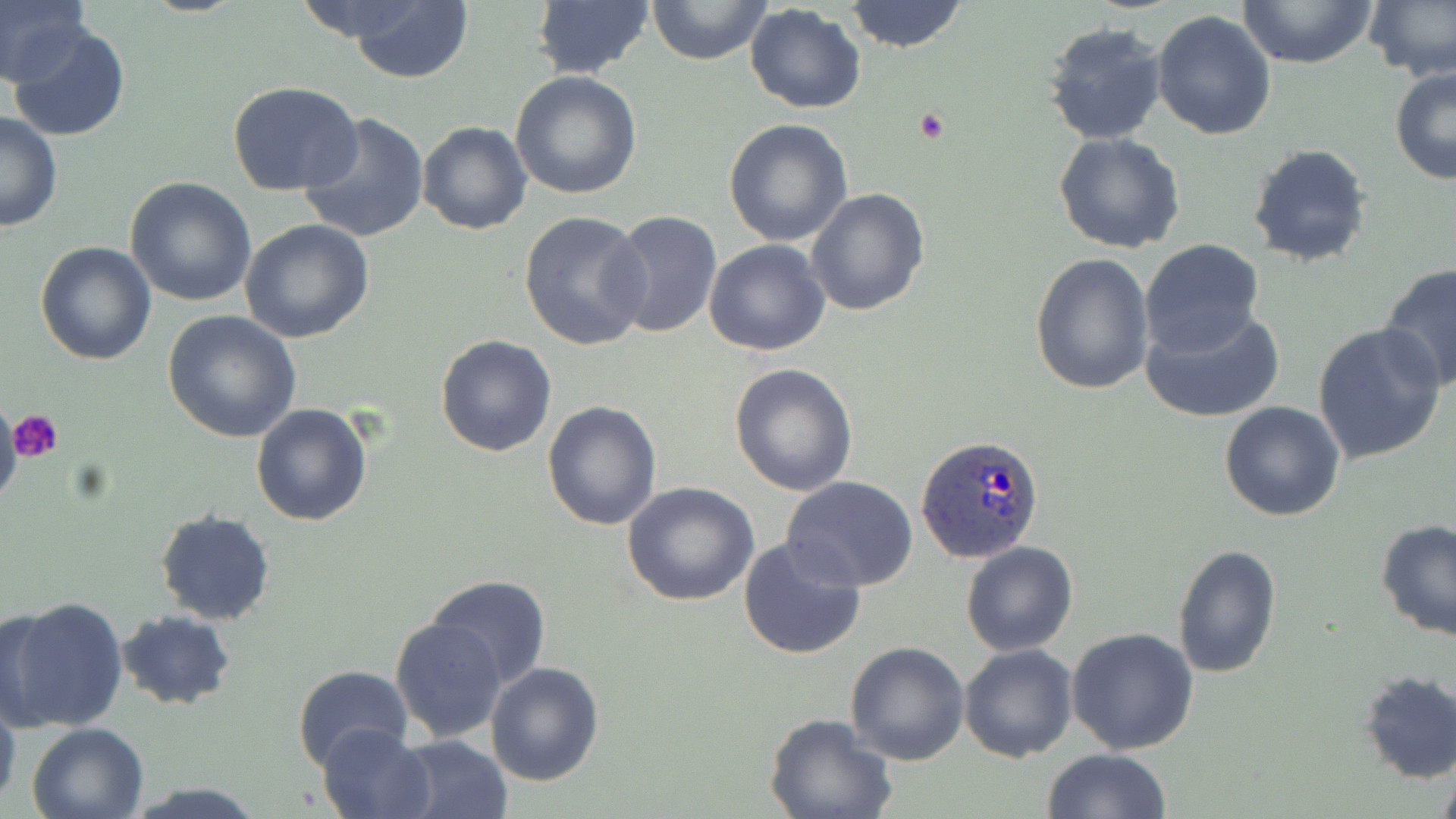
Summary:
  - Coordinate format: approximate bounding boxes as named x1/y1/x2/y2 corners in pixels
  - Plasmodium ovale-infected red blood cell locations: (x1=917, y1=435, x2=1045, y2=565)
  - Uninfected red blood cell locations: (x1=0, y1=0, x2=91, y2=88), (x1=346, y1=0, x2=476, y2=84), (x1=648, y1=0, x2=772, y2=66), (x1=845, y1=0, x2=969, y2=52), (x1=1236, y1=0, x2=1378, y2=69), (x1=1363, y1=0, x2=1456, y2=86), (x1=530, y1=2, x2=654, y2=79), (x1=745, y1=4, x2=867, y2=113), (x1=1150, y1=9, x2=1277, y2=141), (x1=1042, y1=21, x2=1168, y2=144), (x1=8, y1=23, x2=131, y2=141), (x1=1389, y1=67, x2=1456, y2=184), (x1=510, y1=70, x2=642, y2=198), (x1=225, y1=82, x2=366, y2=198), (x1=1, y1=110, x2=62, y2=232), (x1=297, y1=111, x2=430, y2=245), (x1=724, y1=116, x2=853, y2=247), (x1=418, y1=121, x2=532, y2=235), (x1=1053, y1=132, x2=1186, y2=254), (x1=1246, y1=142, x2=1372, y2=269), (x1=125, y1=177, x2=256, y2=305), (x1=806, y1=188, x2=930, y2=316), (x1=519, y1=210, x2=651, y2=351), (x1=607, y1=210, x2=723, y2=338), (x1=240, y1=219, x2=374, y2=343), (x1=703, y1=238, x2=831, y2=357), (x1=1139, y1=238, x2=1264, y2=357), (x1=35, y1=241, x2=156, y2=366), (x1=1029, y1=252, x2=1155, y2=396), (x1=1378, y1=263, x2=1456, y2=393), (x1=1138, y1=303, x2=1289, y2=424), (x1=162, y1=310, x2=302, y2=442), (x1=1312, y1=322, x2=1447, y2=465), (x1=434, y1=333, x2=559, y2=457), (x1=729, y1=363, x2=858, y2=498), (x1=541, y1=400, x2=662, y2=531), (x1=1219, y1=401, x2=1346, y2=520), (x1=251, y1=403, x2=373, y2=528), (x1=783, y1=477, x2=918, y2=590), (x1=622, y1=483, x2=760, y2=607), (x1=154, y1=510, x2=275, y2=626), (x1=1374, y1=518, x2=1456, y2=641), (x1=737, y1=536, x2=868, y2=661), (x1=961, y1=541, x2=1078, y2=657), (x1=1171, y1=544, x2=1284, y2=681), (x1=424, y1=574, x2=552, y2=691), (x1=4, y1=596, x2=130, y2=733), (x1=1, y1=605, x2=52, y2=731), (x1=114, y1=611, x2=235, y2=710), (x1=389, y1=616, x2=507, y2=741), (x1=1066, y1=627, x2=1199, y2=755), (x1=844, y1=641, x2=969, y2=767), (x1=958, y1=643, x2=1079, y2=764), (x1=485, y1=662, x2=605, y2=787), (x1=291, y1=665, x2=415, y2=776), (x1=1356, y1=669, x2=1455, y2=784), (x1=0, y1=693, x2=21, y2=814), (x1=763, y1=713, x2=898, y2=819), (x1=25, y1=721, x2=149, y2=819), (x1=317, y1=722, x2=436, y2=818), (x1=393, y1=735, x2=512, y2=819), (x1=1043, y1=749, x2=1170, y2=819), (x1=125, y1=782, x2=267, y2=818)
  - Platelet locations: (x1=914, y1=109, x2=949, y2=143), (x1=9, y1=408, x2=63, y2=462)
  - Slide-level diagnosis: Plasmodium ovale
  - Image size: 1456×819 pixels
  - Magnification: 1000x
  - Stain: May-Grünwald-Giemsa
  - Preparation: thin blood smear
  - Field of view: single
  - Modality: light microscopy